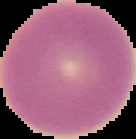
Cell region segmented out of the field of view; the surrounding area is masked to black. Malaria status: uninfected. Image is 136×139 pixels. From a thin blood smear.